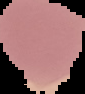 Cell region segmented out of the field of view; the surrounding area is masked to black. Image is 85×94 pixels. Result: no malaria parasites detected. From a thin blood film.